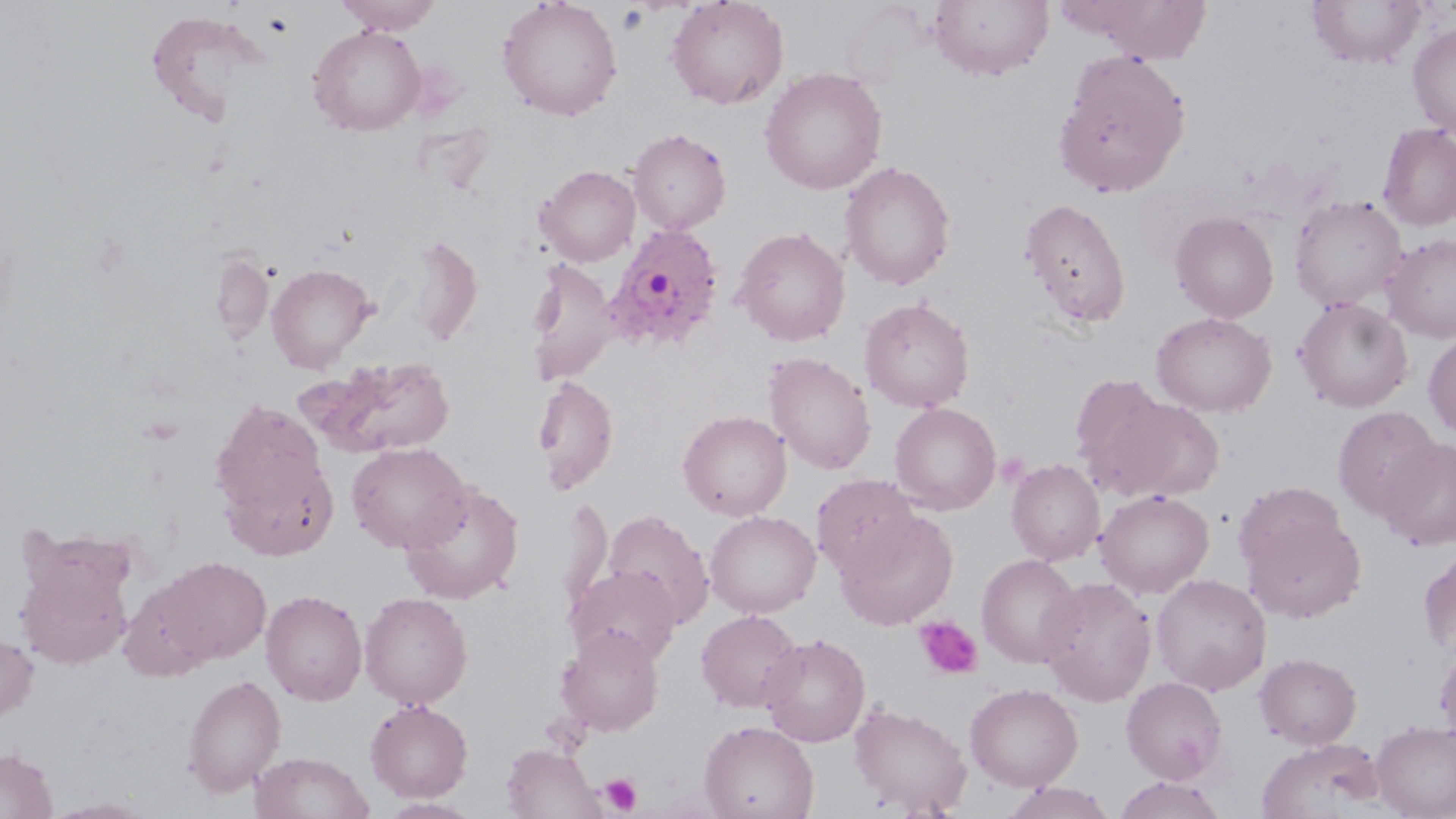
Approximate bounding boxes as (x1,y1)-(x2,y2) corner pairs in pixels. Uninfected red blood cell locations: (335,0)-(442,35), (497,0)-(623,121), (665,0)-(789,109), (1060,0)-(1214,63), (928,1)-(1054,80), (1307,1)-(1428,69), (144,8)-(272,126), (1407,23)-(1456,140), (308,25)-(426,136), (1052,49)-(1191,198), (759,67)-(888,194), (1377,122)-(1456,231), (627,128)-(731,234), (840,160)-(956,290), (535,164)-(640,266), (1289,195)-(1407,311), (1019,197)-(1131,327), (1170,210)-(1279,323), (733,226)-(851,346), (406,232)-(483,347), (1381,234)-(1456,343), (209,251)-(273,343), (525,259)-(620,386), (265,262)-(377,373), (859,297)-(975,413), (1294,297)-(1413,412), (1151,312)-(1277,417), (1423,333)-(1456,439), (764,352)-(876,475), (308,356)-(457,457), (1069,374)-(1173,490), (533,375)-(619,494), (1099,394)-(1226,503), (210,397)-(332,537), (889,402)-(1001,514), (1332,405)-(1442,521), (678,410)-(791,520), (694,410)-(805,619), (1379,437)-(1456,551), (346,442)-(472,553), (1006,458)-(1105,566), (811,474)-(921,578), (399,482)-(525,605), (1094,489)-(1214,599), (1234,494)-(1367,624), (557,495)-(612,619), (836,509)-(958,630), (602,510)-(714,628), (704,510)-(821,618), (15,540)-(137,671), (1418,545)-(1456,656), (977,554)-(1083,668), (157,557)-(271,665), (566,566)-(681,667), (1151,573)-(1272,695), (117,574)-(220,681), (1037,576)-(1157,706), (261,589)-(367,705), (359,591)-(473,708), (695,609)-(804,712), (556,625)-(665,736), (759,632)-(870,747), (0,633)-(39,722), (1434,640)-(1456,746), (1254,652)-(1362,749), (181,673)-(287,797), (1121,677)-(1228,784), (965,682)-(1083,791), (365,698)-(473,802), (849,703)-(972,816), (699,720)-(818,819), (1371,720)-(1456,819), (1256,737)-(1385,819), (501,744)-(604,819), (0,746)-(58,818), (250,751)-(374,819), (1113,776)-(1227,819), (1001,782)-(1119,819), (43,797)-(159,818), (378,797)-(483,818). Plasmodium ovale-infected red blood cell locations: (603,222)-(725,353). Platelet locations: (617,5)-(649,35), (915,616)-(983,679), (601,773)-(642,815). Slide-level diagnosis: Plasmodium ovale. Optical microscopy. Image is 1456×819 pixels. Single field of view. Captured at 1000x magnification. May-Grünwald-Giemsa stain. Thin blood smear.